Locate and identify every blood parasite.
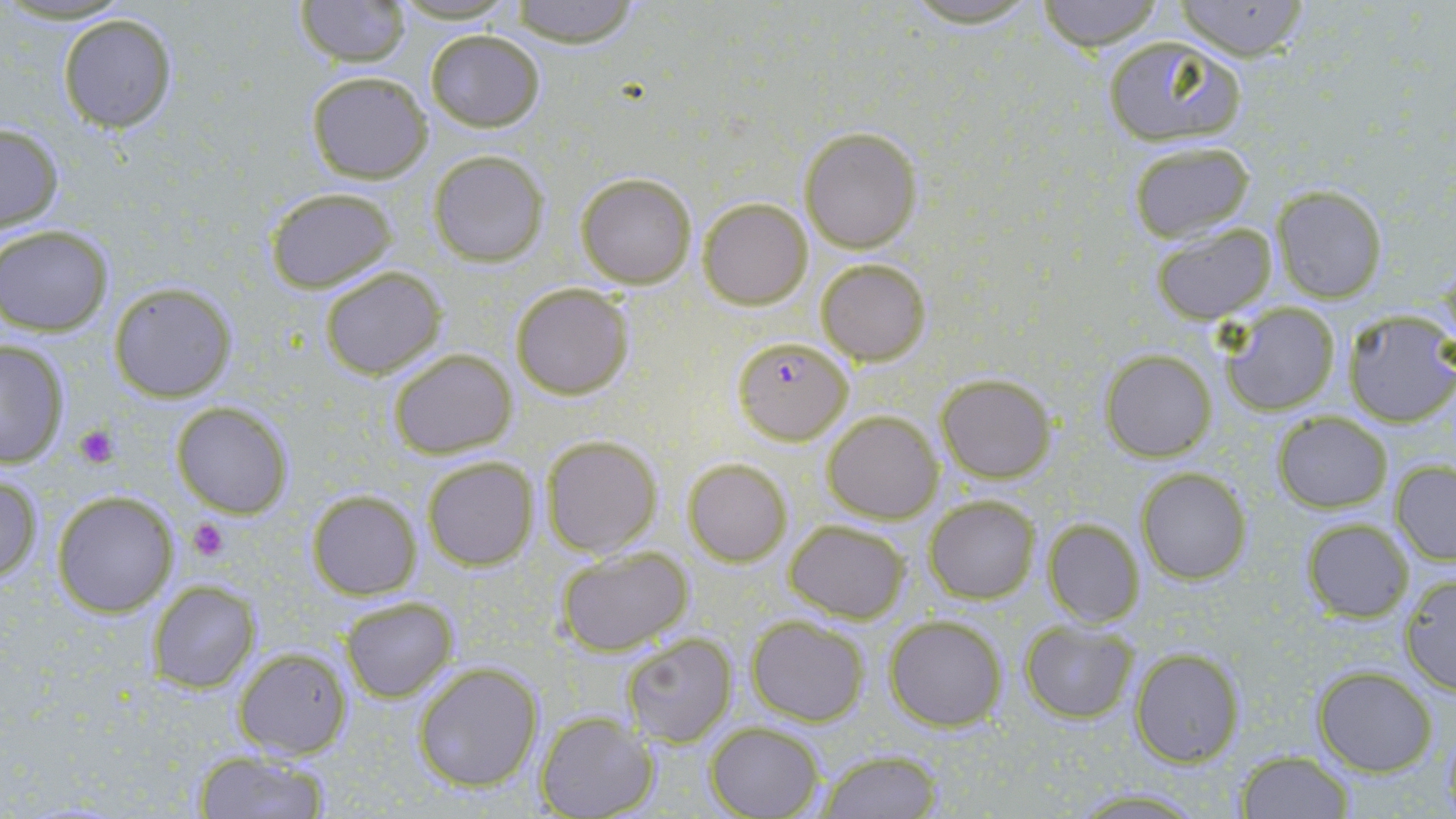
Approximate bounding boxes as [x1, y1, x2, y2] in pixels.
Plasmodium falciparum-infected red blood cells: [732, 336, 854, 445].
No Plasmodium ovale, Plasmodium malariae, Plasmodium vivax, Babesia divergens, or Trypanosoma brucei observed.

Platelet locations: [75, 424, 118, 467], [189, 517, 230, 562]. Uninfected red blood cell locations: [293, 0, 414, 66], [387, 0, 523, 24], [504, 0, 642, 46], [894, 0, 1052, 28], [1034, 0, 1166, 51], [1173, 1, 1311, 60], [57, 13, 179, 134], [424, 30, 545, 131], [1101, 37, 1247, 147], [305, 70, 433, 184], [1, 122, 64, 233], [799, 129, 921, 254], [1127, 141, 1256, 242], [428, 151, 549, 267], [576, 171, 697, 289], [263, 186, 401, 294], [1272, 186, 1388, 303], [698, 198, 812, 309], [1150, 223, 1276, 325], [0, 225, 116, 336], [815, 257, 931, 365], [320, 267, 446, 378], [109, 280, 235, 401], [511, 282, 634, 400], [1219, 303, 1342, 416], [1341, 309, 1456, 426], [0, 338, 72, 465], [388, 348, 516, 458], [1099, 351, 1217, 462], [936, 373, 1056, 481], [170, 401, 293, 518], [822, 410, 943, 524], [1272, 411, 1393, 513], [541, 436, 662, 559], [421, 455, 538, 571], [683, 458, 791, 566], [1391, 460, 1456, 564], [1136, 467, 1251, 585], [0, 472, 42, 584], [50, 490, 178, 617], [307, 491, 421, 599], [924, 495, 1039, 604], [1042, 517, 1146, 628], [783, 519, 910, 621], [1301, 519, 1414, 621], [554, 546, 698, 658], [1398, 572, 1456, 694], [155, 578, 261, 693], [341, 596, 458, 702], [883, 614, 1007, 732], [745, 615, 869, 726], [1019, 622, 1136, 723], [622, 633, 737, 746], [233, 645, 354, 759], [1130, 647, 1244, 766], [412, 661, 544, 792], [1314, 665, 1438, 776], [535, 714, 656, 819], [705, 720, 826, 819], [191, 749, 335, 818], [814, 749, 944, 818], [1237, 750, 1355, 817], [1065, 787, 1213, 816]. Slide-level diagnosis: Plasmodium falciparum. Thin blood film. Single field of view. Image is 1456×819 pixels. May-Grünwald-Giemsa-stained preparation. Captured at 1000x magnification. Optical microscopy.